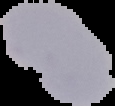

image size = 115×106 pixels
preparation = thin blood film
image type = segmented cell region on a black background
result = negative for Plasmodium parasites